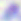 Toxoplasma gondii is seen. Captured at 400x magnification. Micrograph.